Report the malaria status of this cell.
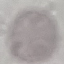

It is uninfected.

image_type: cell patch, automatically extracted from a larger field of view and resized to 64 × 64 pixels
stain: Giemsa
preparation: thin smear
capture: smartphone camera at the microscope eyepiece